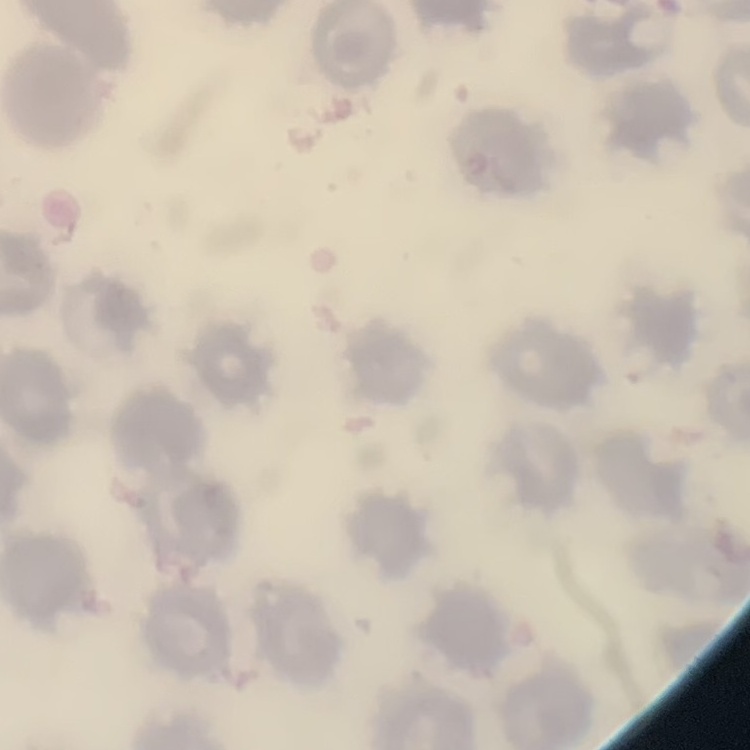

red blood cell morphology = no rouleaux formation
image type = square crop of a larger photomicrograph
stain = Field's or Giemsa
preparation = thin blood smear